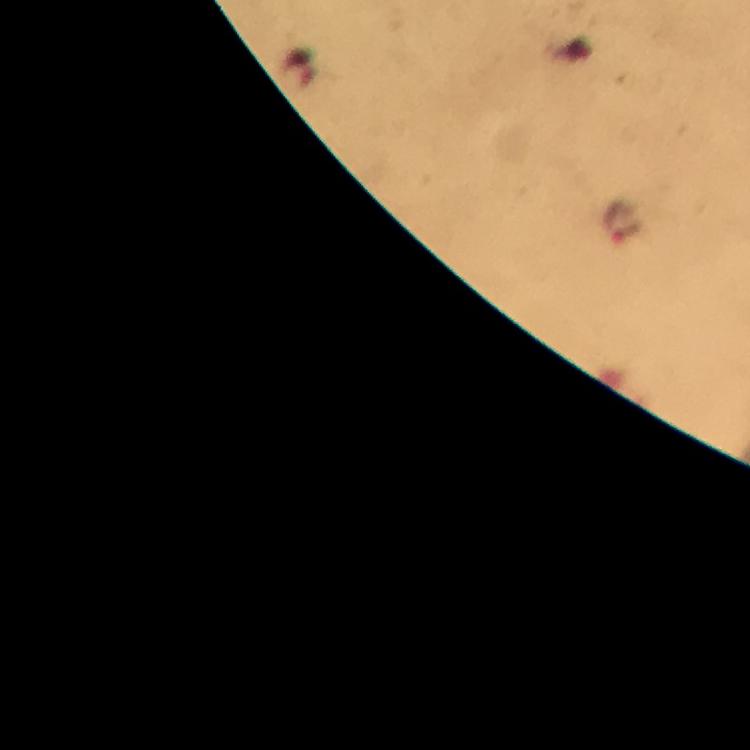
context = from a diagnostic examination for malaria
preparation = thick smear
stain = Giemsa
cropped from = one field of view
malaria parasite locations = approximate centers as (x, y) in pixels: (623, 223)
immersion oil = used
capture = smartphone camera through the microscope
magnification = 100x
image size = 750×750 pixels